Report the malaria status of this cell.
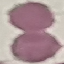

It is uninfected.

Summary:
  - Capture: smartphone camera at the microscope eyepiece
  - Stain: Giemsa
  - Preparation: thin smear
  - Image type: automatically extracted cell patch, resized to 64 × 64 pixels